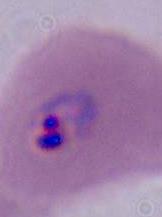

Summary:
  - Modality: micrograph
  - Magnification: 400x or 1000x
  - Identification: Plasmodium